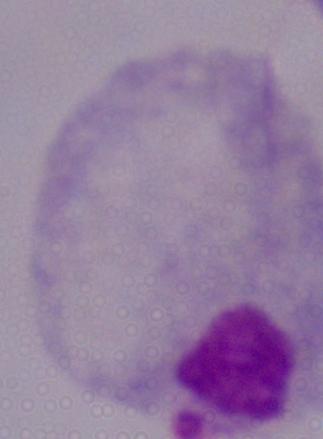

A trichomonad is shown. Captured at 1000x magnification. Micrograph.